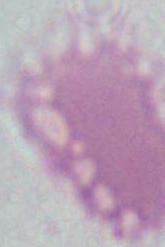
Summary:
  - Modality: photomicrograph
  - Magnification: 1000x
  - Identification: red blood cell